Locate every blood parasite and identify its species.
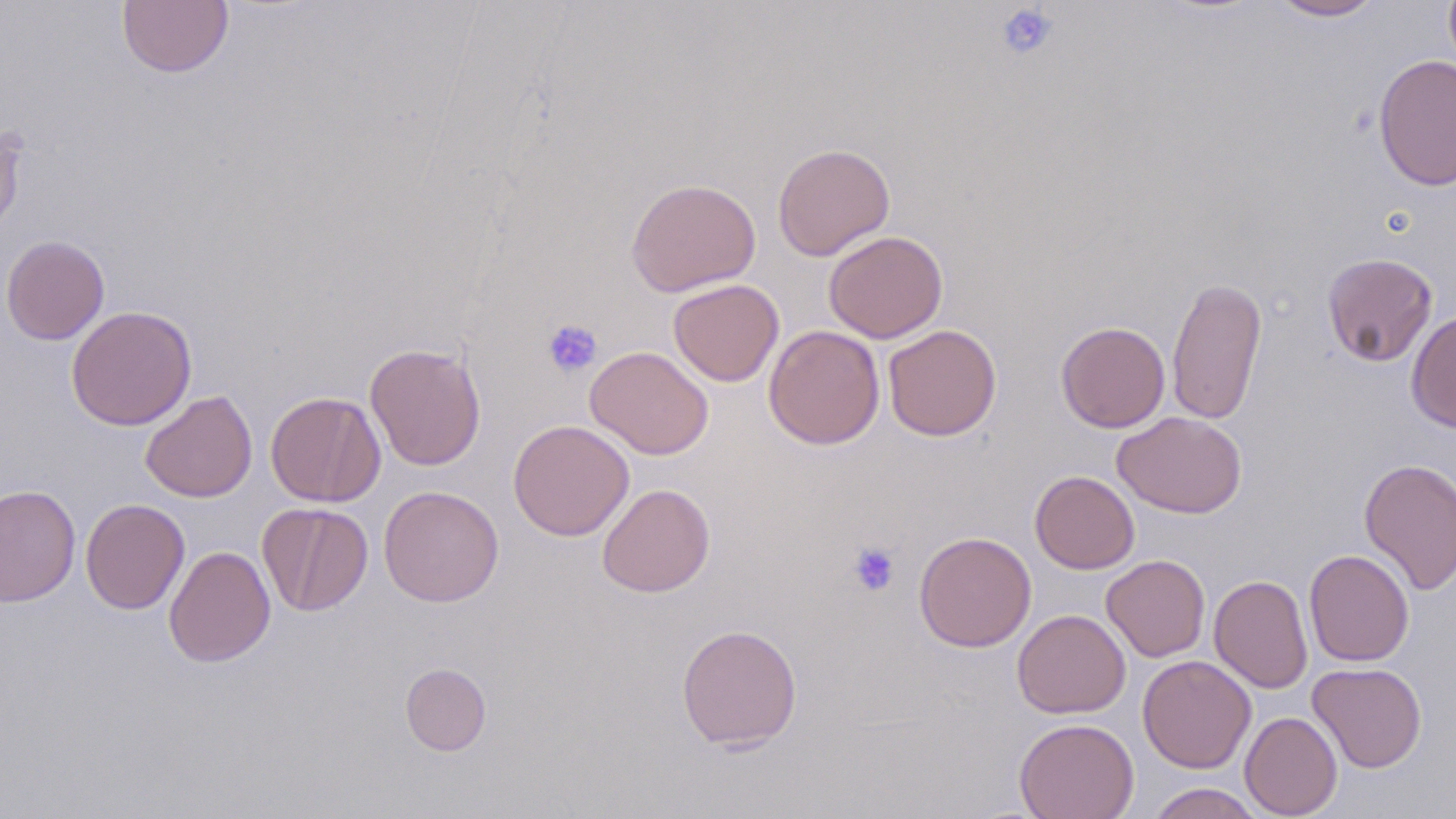

No blood parasites observed.

slide_level_diagnosis: no evidence of blood parasites
magnification: 1000x
platelet_locations: 'approximate bounding boxes as named x1/y1/x2/y2 corners in pixels: (x1=996, y1=3, x2=1059, y2=59), (x1=542, y1=318, x2=603, y2=378), (x1=847, y1=541, x2=900, y2=596)'
field_of_view: single
modality: light microscopy
preparation: thin blood film
stain: May-Grünwald-Giemsa
uninfected_red_blood_cell_locations: 'approximate bounding boxes as named x1/y1/x2/y2 corners in pixels: (x1=117, y1=0, x2=233, y2=78), (x1=1268, y1=0, x2=1385, y2=21), (x1=1374, y1=54, x2=1456, y2=191), (x1=0, y1=123, x2=29, y2=249), (x1=772, y1=143, x2=895, y2=261), (x1=626, y1=177, x2=762, y2=297), (x1=823, y1=230, x2=949, y2=343), (x1=0, y1=235, x2=110, y2=345), (x1=1322, y1=252, x2=1438, y2=367), (x1=1166, y1=274, x2=1267, y2=426), (x1=668, y1=278, x2=784, y2=386), (x1=66, y1=305, x2=197, y2=431), (x1=1406, y1=308, x2=1456, y2=433), (x1=1056, y1=321, x2=1170, y2=433), (x1=764, y1=324, x2=885, y2=450), (x1=883, y1=324, x2=1002, y2=441), (x1=365, y1=342, x2=486, y2=471), (x1=585, y1=346, x2=714, y2=460), (x1=140, y1=390, x2=258, y2=502), (x1=266, y1=391, x2=385, y2=507), (x1=1113, y1=411, x2=1248, y2=519), (x1=508, y1=419, x2=635, y2=541), (x1=1359, y1=456, x2=1456, y2=596), (x1=1029, y1=470, x2=1140, y2=574), (x1=597, y1=483, x2=715, y2=597), (x1=0, y1=484, x2=81, y2=608), (x1=378, y1=486, x2=504, y2=607), (x1=80, y1=498, x2=189, y2=614), (x1=257, y1=502, x2=373, y2=616), (x1=913, y1=531, x2=1036, y2=652), (x1=164, y1=545, x2=276, y2=668), (x1=1304, y1=550, x2=1415, y2=666), (x1=1101, y1=555, x2=1210, y2=662), (x1=1209, y1=574, x2=1313, y2=694), (x1=1012, y1=609, x2=1131, y2=718), (x1=676, y1=623, x2=802, y2=751), (x1=1137, y1=654, x2=1256, y2=773), (x1=1307, y1=661, x2=1427, y2=773), (x1=400, y1=663, x2=491, y2=755), (x1=1240, y1=711, x2=1343, y2=818), (x1=1015, y1=717, x2=1140, y2=819), (x1=1145, y1=783, x2=1265, y2=818)'
image_size: 1456×819 pixels